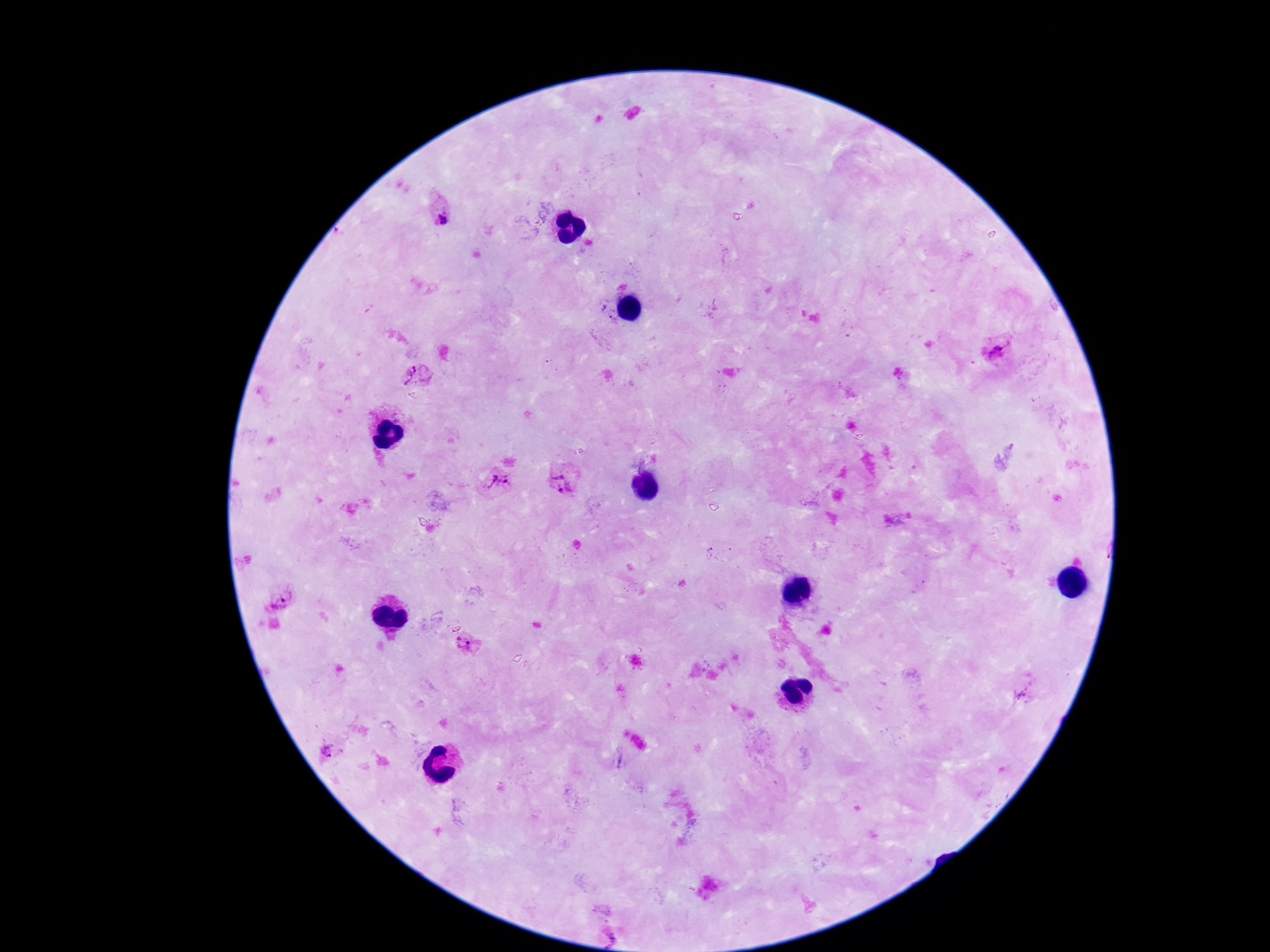
{
  "patient_malaria_status": "infected",
  "field_of_view": "single",
  "capture": "smartphone camera through the microscope eyepiece",
  "preparation": "thick blood smear",
  "plasmodium_parasite_locations": "approximate centers as (x, y) in pixels: (442, 209), (998, 351), (416, 377), (564, 478), (497, 484), (468, 643), (325, 752)",
  "image_size": "1270×952 pixels",
  "stain": "Giemsa",
  "magnification": "100x"
}